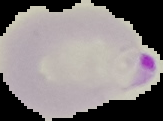
Summary:
  - Result: malaria parasites detected
  - Preparation: thin blood film
  - Image type: segmented cell region with the area outside set to black
  - Image size: 163×121 pixels